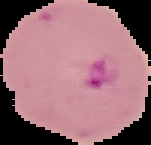
Summary:
  - Image size: 151×145 pixels
  - Image type: segmented cell region with the area outside set to black
  - Result: malaria parasites identified
  - Preparation: thin blood smear